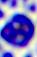
Summary:
  - Modality: photomicrograph
  - Identification: leukocyte
  - Magnification: 400x